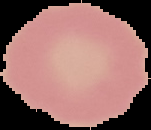 From a thin blood smear. Result: no Plasmodium parasites detected. Cell region segmented out of the field of view; the surrounding area is masked to black. Image is 151×130 pixels.